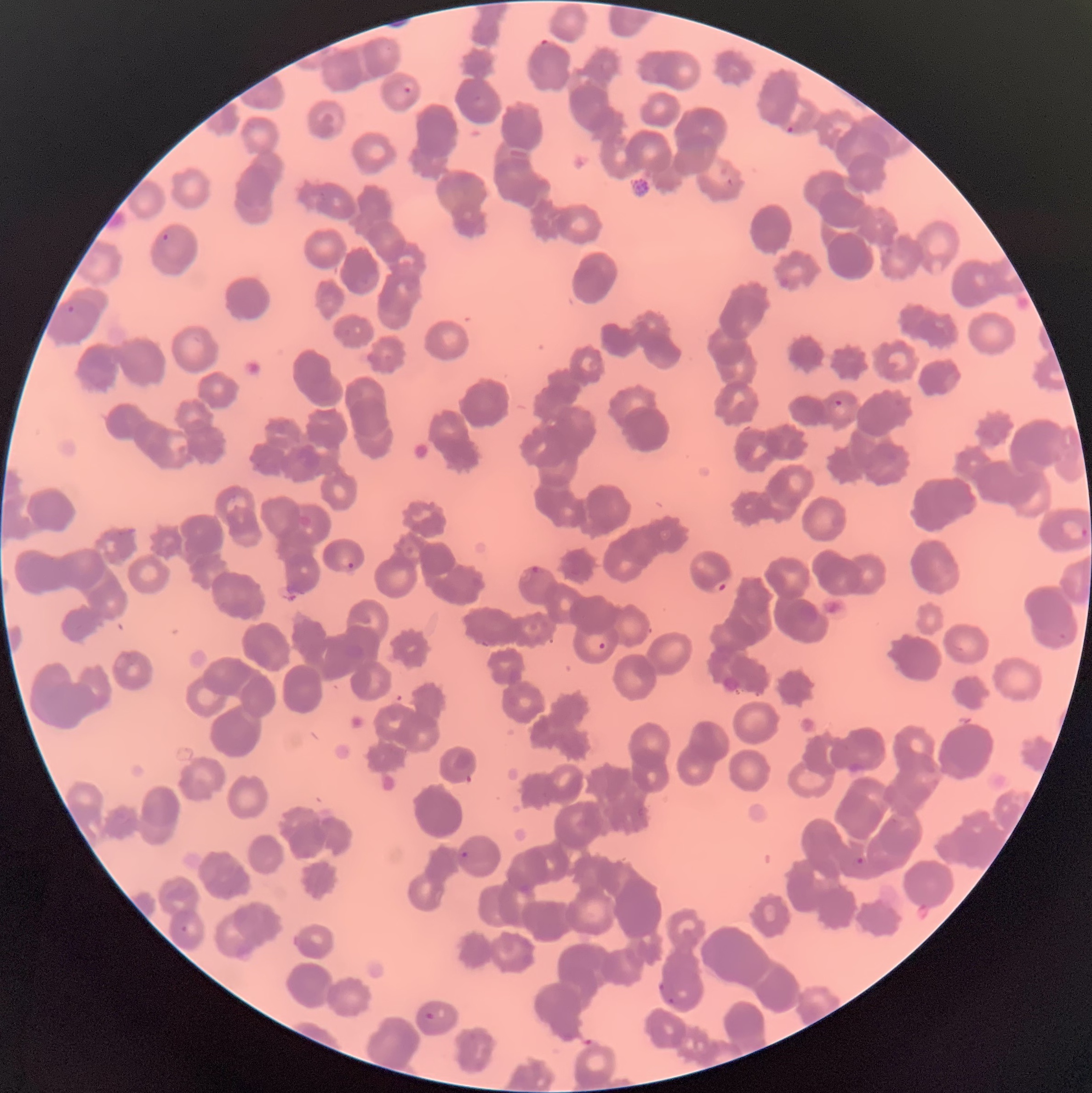
Approximate bounding boxes as (x1,y1)-(x2,y2) corner pairs in pixels. Plasmodium parasite locations: (539,38)-(552,52), (404,86)-(412,94), (472,94)-(483,103), (787,123)-(795,133), (163,234)-(173,241), (67,304)-(81,314), (833,400)-(843,408), (1061,516)-(1092,542), (347,562)-(355,569), (534,564)-(547,575), (712,580)-(727,592), (598,642)-(607,649), (459,849)-(469,862), (852,855)-(868,869), (180,925)-(189,933), (657,984)-(668,993), (668,996)-(676,1005), (424,1012)-(436,1021). Thin blood film. Optical microscopy. Image is 1092×1093 pixels. The red blood cells show rouleaux formation.